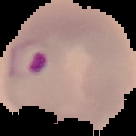

Summary:
  - Image type: cell region segmented out of the field of view; surrounding area masked to black
  - Image size: 136×136 pixels
  - Preparation: thin blood smear
  - Malaria status: parasitized